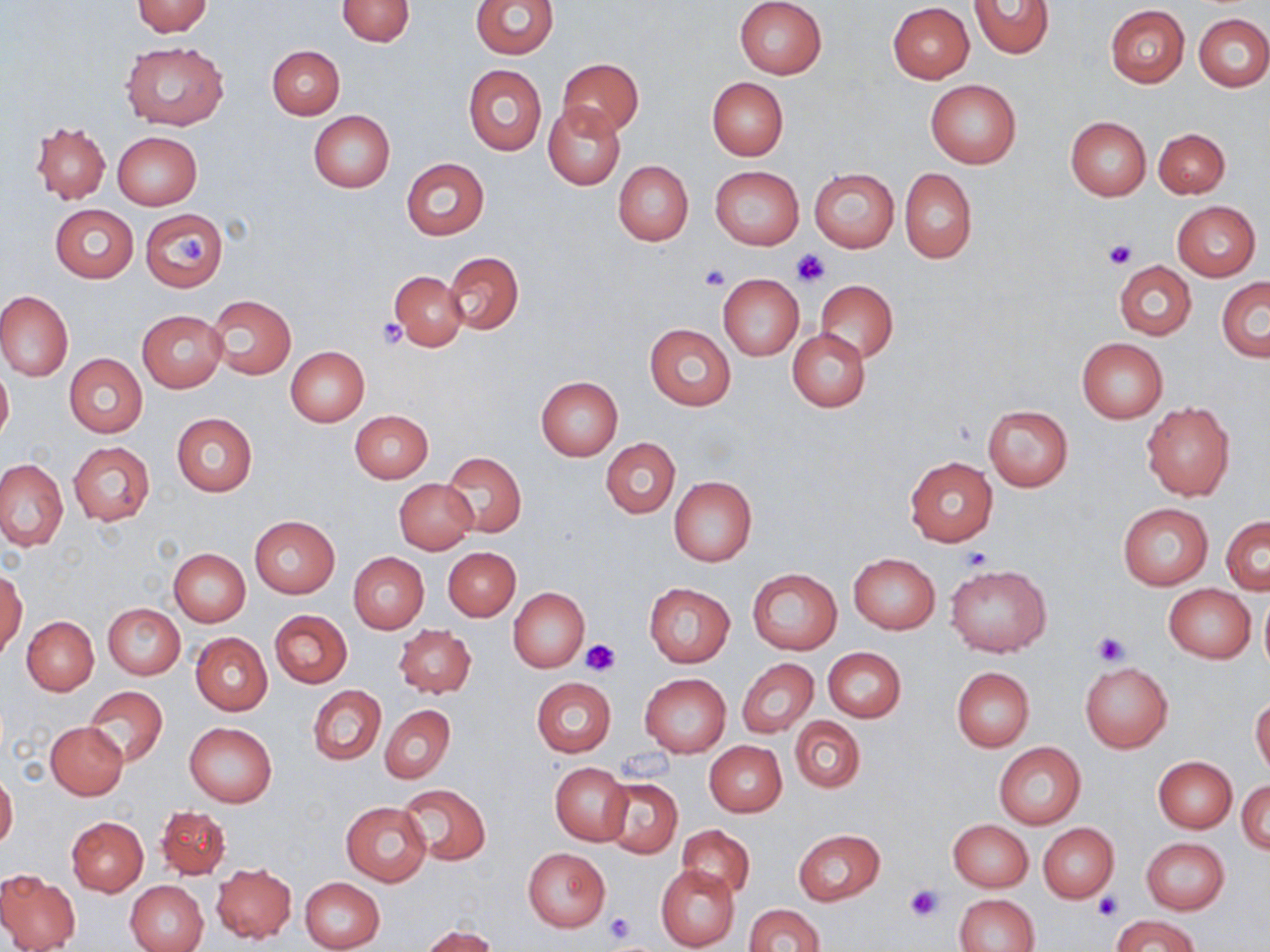

Summary:
  - Coordinate format: approximate bounding boxes as named x1/y1/x2/y2 corners in pixels
  - Uninfected red blood cell locations: (x1=472, y1=0, x2=558, y2=58), (x1=734, y1=0, x2=828, y2=79), (x1=131, y1=1, x2=214, y2=36), (x1=337, y1=1, x2=415, y2=46), (x1=968, y1=1, x2=1053, y2=60), (x1=888, y1=3, x2=975, y2=83), (x1=1105, y1=4, x2=1189, y2=87), (x1=1194, y1=13, x2=1269, y2=92), (x1=122, y1=42, x2=229, y2=130), (x1=267, y1=46, x2=345, y2=119), (x1=557, y1=58, x2=643, y2=137), (x1=463, y1=65, x2=546, y2=155), (x1=707, y1=78, x2=787, y2=159), (x1=925, y1=78, x2=1022, y2=168), (x1=543, y1=103, x2=626, y2=189), (x1=309, y1=111, x2=395, y2=193), (x1=1065, y1=116, x2=1151, y2=200), (x1=31, y1=120, x2=110, y2=203), (x1=1154, y1=128, x2=1230, y2=198), (x1=113, y1=131, x2=202, y2=210), (x1=402, y1=157, x2=489, y2=239), (x1=613, y1=160, x2=694, y2=246), (x1=711, y1=166, x2=805, y2=250), (x1=809, y1=168, x2=899, y2=253), (x1=900, y1=169, x2=977, y2=263), (x1=1172, y1=201, x2=1261, y2=281), (x1=51, y1=205, x2=138, y2=282), (x1=140, y1=208, x2=229, y2=291), (x1=443, y1=251, x2=524, y2=334), (x1=1113, y1=260, x2=1196, y2=340), (x1=391, y1=271, x2=468, y2=352), (x1=717, y1=273, x2=804, y2=360), (x1=1217, y1=278, x2=1270, y2=361), (x1=814, y1=280, x2=898, y2=363), (x1=0, y1=291, x2=72, y2=380), (x1=207, y1=296, x2=296, y2=379), (x1=137, y1=310, x2=227, y2=393), (x1=645, y1=324, x2=737, y2=411), (x1=787, y1=329, x2=870, y2=412), (x1=1076, y1=338, x2=1168, y2=422), (x1=286, y1=346, x2=370, y2=425), (x1=64, y1=354, x2=147, y2=438), (x1=0, y1=366, x2=13, y2=447), (x1=535, y1=376, x2=623, y2=460), (x1=1141, y1=402, x2=1235, y2=500), (x1=983, y1=405, x2=1073, y2=490), (x1=350, y1=410, x2=432, y2=482), (x1=172, y1=413, x2=257, y2=496), (x1=602, y1=438, x2=679, y2=517), (x1=68, y1=442, x2=155, y2=525), (x1=440, y1=451, x2=526, y2=538), (x1=905, y1=457, x2=998, y2=546), (x1=0, y1=459, x2=67, y2=550), (x1=669, y1=476, x2=757, y2=566), (x1=393, y1=479, x2=477, y2=554), (x1=1117, y1=504, x2=1214, y2=589), (x1=249, y1=516, x2=340, y2=599), (x1=1222, y1=516, x2=1269, y2=594), (x1=443, y1=547, x2=520, y2=621), (x1=170, y1=548, x2=250, y2=626), (x1=348, y1=552, x2=429, y2=634), (x1=849, y1=554, x2=939, y2=634), (x1=947, y1=563, x2=1050, y2=658), (x1=748, y1=568, x2=841, y2=655), (x1=1, y1=569, x2=27, y2=660), (x1=643, y1=581, x2=735, y2=668), (x1=1164, y1=584, x2=1255, y2=663), (x1=509, y1=588, x2=589, y2=671), (x1=1259, y1=590, x2=1270, y2=678), (x1=103, y1=603, x2=185, y2=679), (x1=271, y1=610, x2=352, y2=688), (x1=22, y1=617, x2=98, y2=695), (x1=394, y1=625, x2=477, y2=697), (x1=190, y1=632, x2=273, y2=714), (x1=823, y1=647, x2=906, y2=722), (x1=738, y1=659, x2=818, y2=737), (x1=1080, y1=662, x2=1173, y2=754), (x1=952, y1=667, x2=1035, y2=751), (x1=640, y1=674, x2=730, y2=756), (x1=532, y1=677, x2=616, y2=757), (x1=84, y1=686, x2=168, y2=766), (x1=308, y1=686, x2=385, y2=764), (x1=1251, y1=697, x2=1270, y2=775), (x1=380, y1=704, x2=454, y2=785), (x1=791, y1=717, x2=864, y2=793), (x1=45, y1=722, x2=129, y2=799), (x1=184, y1=723, x2=277, y2=806), (x1=705, y1=741, x2=787, y2=818), (x1=993, y1=742, x2=1086, y2=828), (x1=1153, y1=756, x2=1236, y2=832), (x1=550, y1=762, x2=632, y2=845), (x1=0, y1=771, x2=18, y2=850), (x1=601, y1=778, x2=683, y2=858), (x1=1237, y1=781, x2=1270, y2=855), (x1=397, y1=783, x2=491, y2=865), (x1=340, y1=802, x2=431, y2=887), (x1=156, y1=806, x2=230, y2=881), (x1=67, y1=816, x2=148, y2=895), (x1=948, y1=820, x2=1032, y2=892), (x1=1037, y1=822, x2=1118, y2=903), (x1=678, y1=824, x2=756, y2=898), (x1=793, y1=829, x2=885, y2=905), (x1=1141, y1=837, x2=1230, y2=915), (x1=523, y1=846, x2=611, y2=933), (x1=212, y1=864, x2=295, y2=943), (x1=656, y1=864, x2=739, y2=952), (x1=0, y1=870, x2=81, y2=952), (x1=299, y1=876, x2=386, y2=952), (x1=125, y1=880, x2=208, y2=952), (x1=955, y1=893, x2=1039, y2=952), (x1=742, y1=903, x2=825, y2=952), (x1=1114, y1=914, x2=1197, y2=952), (x1=422, y1=926, x2=499, y2=952)
  - Platelet locations: (x1=174, y1=233, x2=208, y2=267), (x1=1105, y1=240, x2=1136, y2=270), (x1=792, y1=249, x2=831, y2=286), (x1=698, y1=265, x2=730, y2=291), (x1=375, y1=320, x2=409, y2=349), (x1=960, y1=548, x2=992, y2=571), (x1=1089, y1=631, x2=1131, y2=667), (x1=579, y1=641, x2=618, y2=678), (x1=905, y1=884, x2=942, y2=920), (x1=1092, y1=893, x2=1122, y2=921), (x1=603, y1=912, x2=634, y2=945)
  - Slide-level diagnosis: no evidence of blood parasites
  - Stain: May-Grünwald-Giemsa
  - Image size: 1270×952 pixels
  - Modality: light microscopy
  - Preparation: thin blood film
  - Field of view: one of a larger specimen
  - Magnification: 1000x